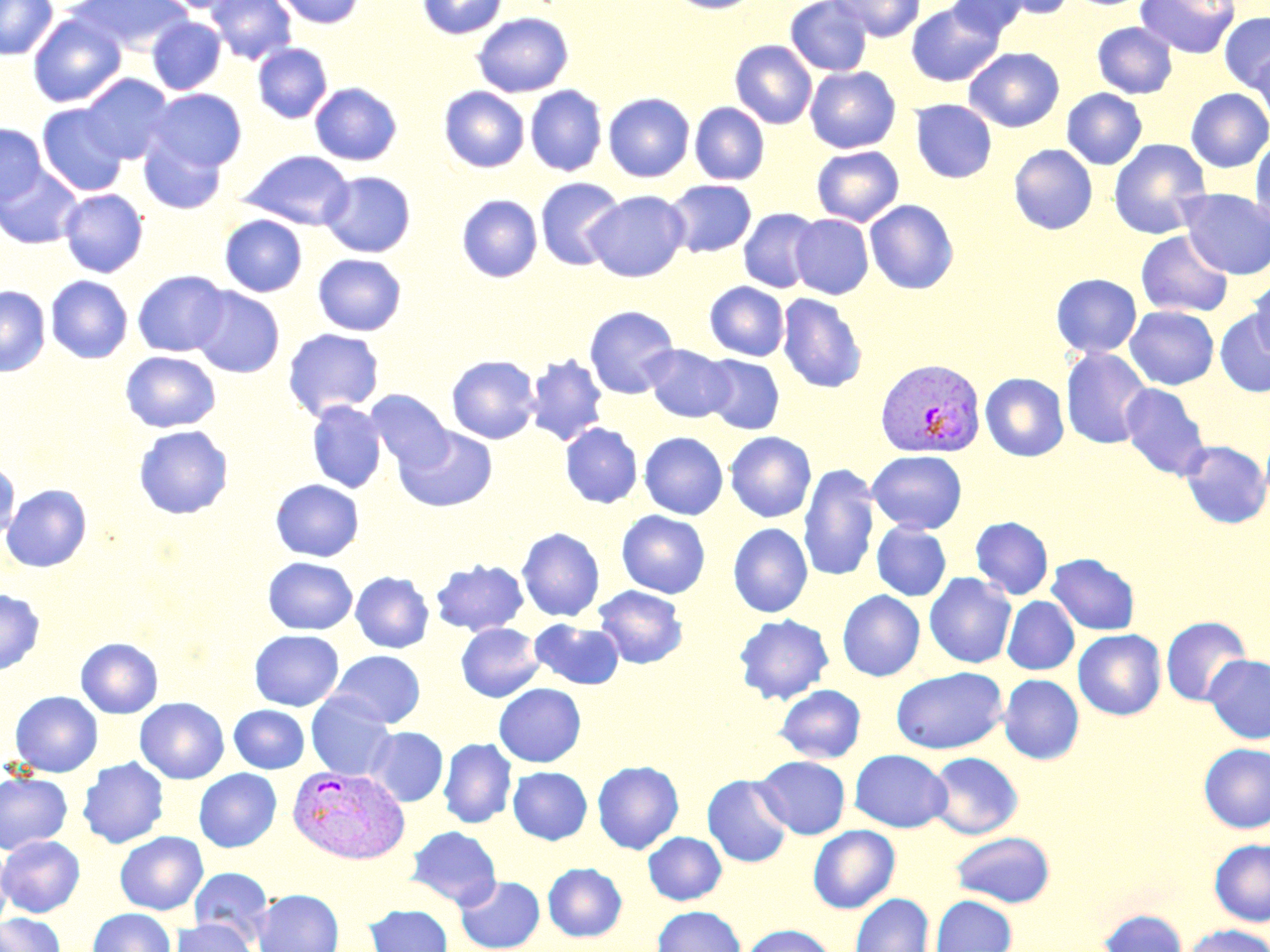

Approximate bounding boxes as [x1, y1, x2, y2] in pixels. Plasmodium vivax-infected red blood cell locations: [876, 359, 985, 458], [288, 764, 410, 864]. Uninfected red blood cell locations: [0, 0, 57, 60], [70, 0, 192, 54], [156, 0, 244, 13], [206, 0, 297, 64], [274, 0, 364, 28], [417, 0, 508, 39], [669, 0, 762, 14], [785, 0, 873, 76], [948, 0, 1030, 40], [992, 0, 1078, 19], [1135, 0, 1240, 59], [832, 1, 925, 41], [906, 2, 1005, 87], [471, 12, 573, 97], [1220, 12, 1270, 92], [28, 13, 126, 108], [147, 17, 226, 94], [1092, 21, 1178, 98], [730, 40, 817, 129], [253, 43, 332, 123], [1250, 46, 1270, 131], [964, 47, 1064, 132], [805, 66, 901, 153], [80, 74, 174, 163], [310, 82, 402, 166], [525, 85, 607, 176], [439, 87, 529, 173], [1062, 88, 1147, 169], [1186, 88, 1270, 172], [148, 89, 247, 172], [603, 93, 695, 182], [910, 99, 997, 183], [689, 102, 770, 185], [38, 104, 128, 197], [0, 123, 47, 205], [138, 133, 227, 214], [1250, 135, 1270, 228], [1108, 138, 1211, 239], [1009, 144, 1097, 234], [812, 146, 904, 226], [238, 150, 354, 230], [0, 165, 82, 249], [320, 170, 416, 258], [535, 177, 626, 271], [664, 180, 757, 257], [59, 189, 148, 277], [1179, 189, 1270, 279], [584, 190, 690, 281], [456, 194, 543, 282], [865, 199, 959, 294], [738, 208, 822, 293], [790, 214, 874, 299], [220, 215, 307, 297], [1136, 230, 1234, 318], [313, 254, 406, 335], [132, 270, 230, 357], [1051, 273, 1141, 358], [46, 275, 133, 363], [1247, 276, 1270, 360], [705, 281, 790, 361], [0, 286, 50, 376], [191, 287, 285, 378], [777, 293, 867, 393], [583, 305, 680, 399], [1125, 305, 1219, 390], [1215, 310, 1270, 397], [282, 328, 385, 420], [643, 345, 735, 422], [1061, 347, 1153, 449], [121, 351, 220, 432], [524, 354, 608, 446], [701, 354, 784, 434], [446, 355, 541, 444], [980, 372, 1069, 461], [1120, 383, 1211, 480], [367, 390, 453, 471], [306, 400, 387, 493], [560, 422, 642, 508], [134, 425, 233, 518], [395, 426, 497, 511], [725, 431, 816, 522], [639, 432, 728, 519], [1180, 440, 1270, 529], [867, 450, 967, 533], [0, 461, 20, 541], [798, 463, 880, 581], [270, 479, 364, 562], [2, 484, 91, 572], [616, 510, 710, 598], [971, 516, 1053, 599], [871, 522, 951, 601], [728, 523, 813, 617], [517, 528, 604, 622], [1047, 553, 1140, 635], [263, 556, 358, 635], [431, 559, 528, 635], [351, 572, 434, 653], [924, 572, 1016, 668], [593, 585, 688, 669], [0, 589, 45, 675], [837, 590, 925, 681], [1002, 596, 1079, 674], [734, 613, 834, 704], [1161, 616, 1251, 706], [530, 619, 625, 690], [456, 622, 545, 702], [1073, 629, 1166, 720], [250, 630, 344, 711], [76, 637, 163, 718], [329, 650, 425, 728], [1204, 654, 1270, 744], [891, 667, 1007, 754], [998, 674, 1084, 764], [494, 683, 586, 767], [775, 684, 866, 763], [10, 691, 103, 777], [306, 692, 396, 781], [135, 697, 229, 784], [229, 705, 309, 773], [365, 726, 448, 806], [438, 738, 517, 828], [1198, 743, 1270, 833], [850, 749, 951, 832], [927, 752, 1023, 839], [755, 756, 850, 838], [77, 757, 169, 849], [592, 760, 684, 854], [508, 766, 592, 844], [194, 769, 281, 852], [0, 772, 72, 854], [702, 774, 794, 867], [407, 825, 501, 909], [808, 825, 900, 913], [115, 831, 208, 915], [644, 831, 727, 905], [951, 831, 1056, 907], [0, 835, 85, 917], [1209, 838, 1270, 926], [0, 843, 13, 932], [543, 863, 627, 942], [189, 867, 273, 945], [455, 875, 544, 952], [252, 889, 344, 952], [850, 893, 933, 952], [930, 895, 1017, 952], [366, 904, 452, 952], [652, 905, 745, 952], [88, 908, 175, 952], [1098, 908, 1188, 952], [0, 913, 64, 952], [172, 918, 256, 952], [741, 924, 838, 952], [1179, 924, 1270, 952]. Slide-level diagnosis: Plasmodium vivax. Thin blood film. Optical microscopy. Single field of view. Captured at 1000x magnification. May-Grünwald-Giemsa stain. Image is 1270×952 pixels.